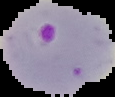

Summary:
  - Result: Plasmodium parasites detected
  - Preparation: thin blood smear
  - Image size: 115×97 pixels
  - Image type: segmented cell region with the area outside set to black